Assess the morphology of the erythrocytes.
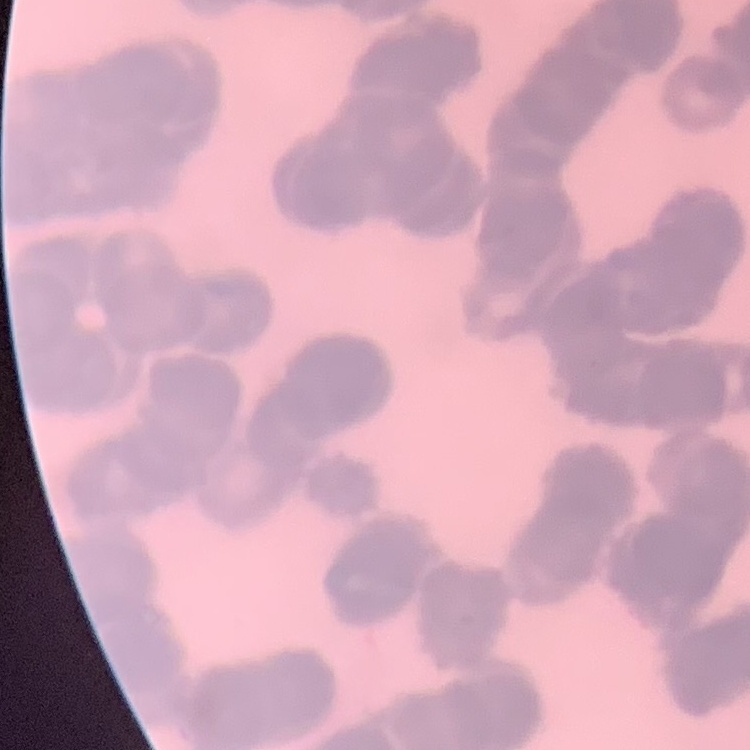
They show rouleaux formation.

Summary:
  - Preparation: thin blood smear
  - Image type: square crop of a larger photomicrograph
  - Stain: Field's or Giemsa